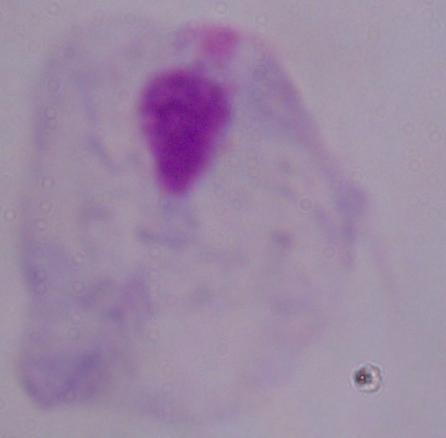

modality = photomicrograph
identification = trichomonad
magnification = 1000x